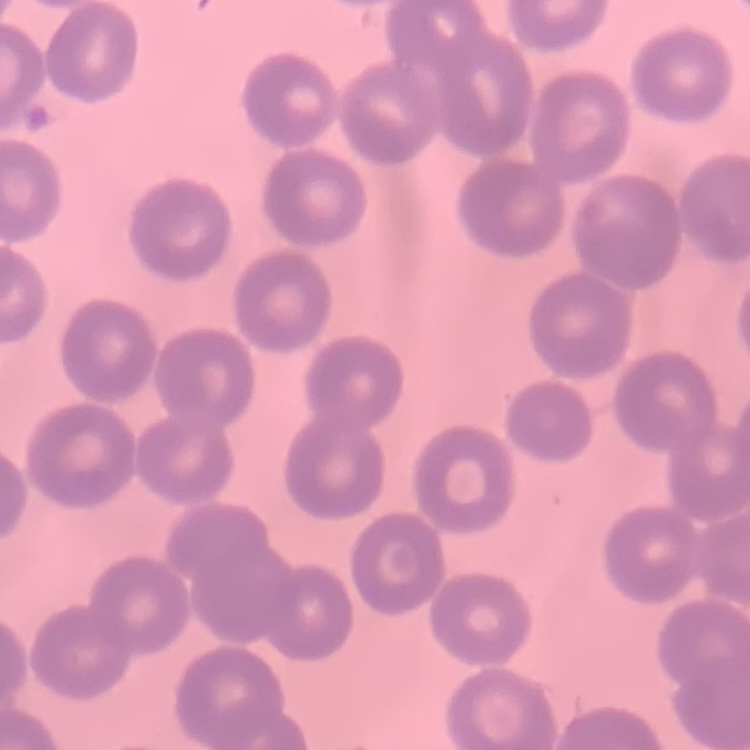
The red blood cells show no rouleaux formation. Stained with either Field's or Giemsa. One tile cut from a larger photomicrograph. Thin blood film.